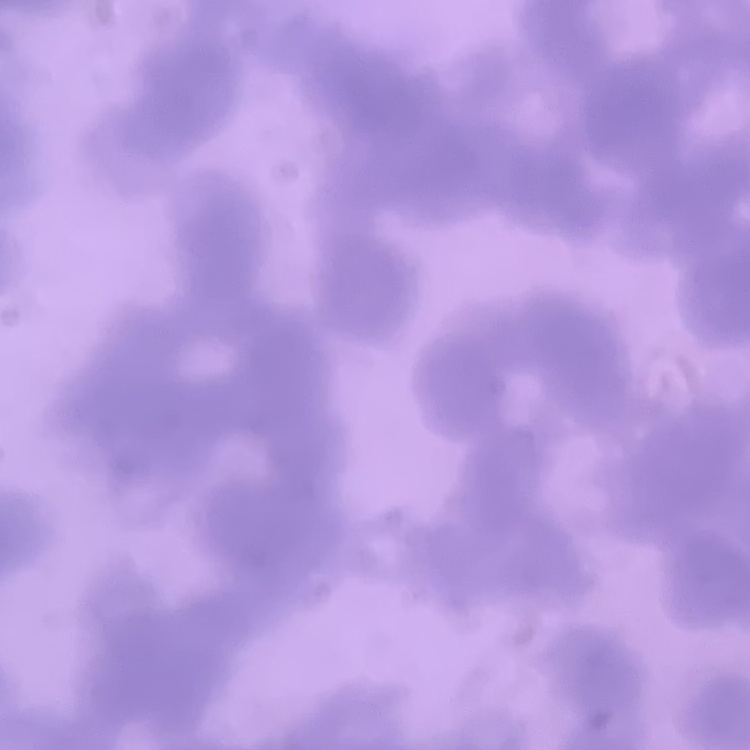

The erythrocytes show rouleaux formation. Thin blood film. One tile cut from a larger photomicrograph. Stained with either Field's or Giemsa.